Classify this cell by malaria status.
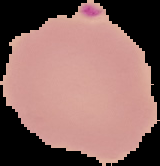
Parasitized.

From a thin blood film. Cell region segmented out of the field of view; the surrounding area is masked to black. Image is 160×166 pixels.